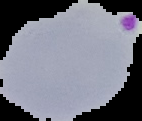
Image is 142×121 pixels. Result: Plasmodium parasites detected. From a thin blood film. Cell region segmented out of the field of view; the surrounding area is masked to black.